Classify this cell by malaria status.
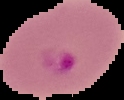

Parasitized.

image size = 124×100 pixels
image type = cell region segmented out of the field of view; surrounding area masked to black
preparation = thin blood film